Identify the preparation type.
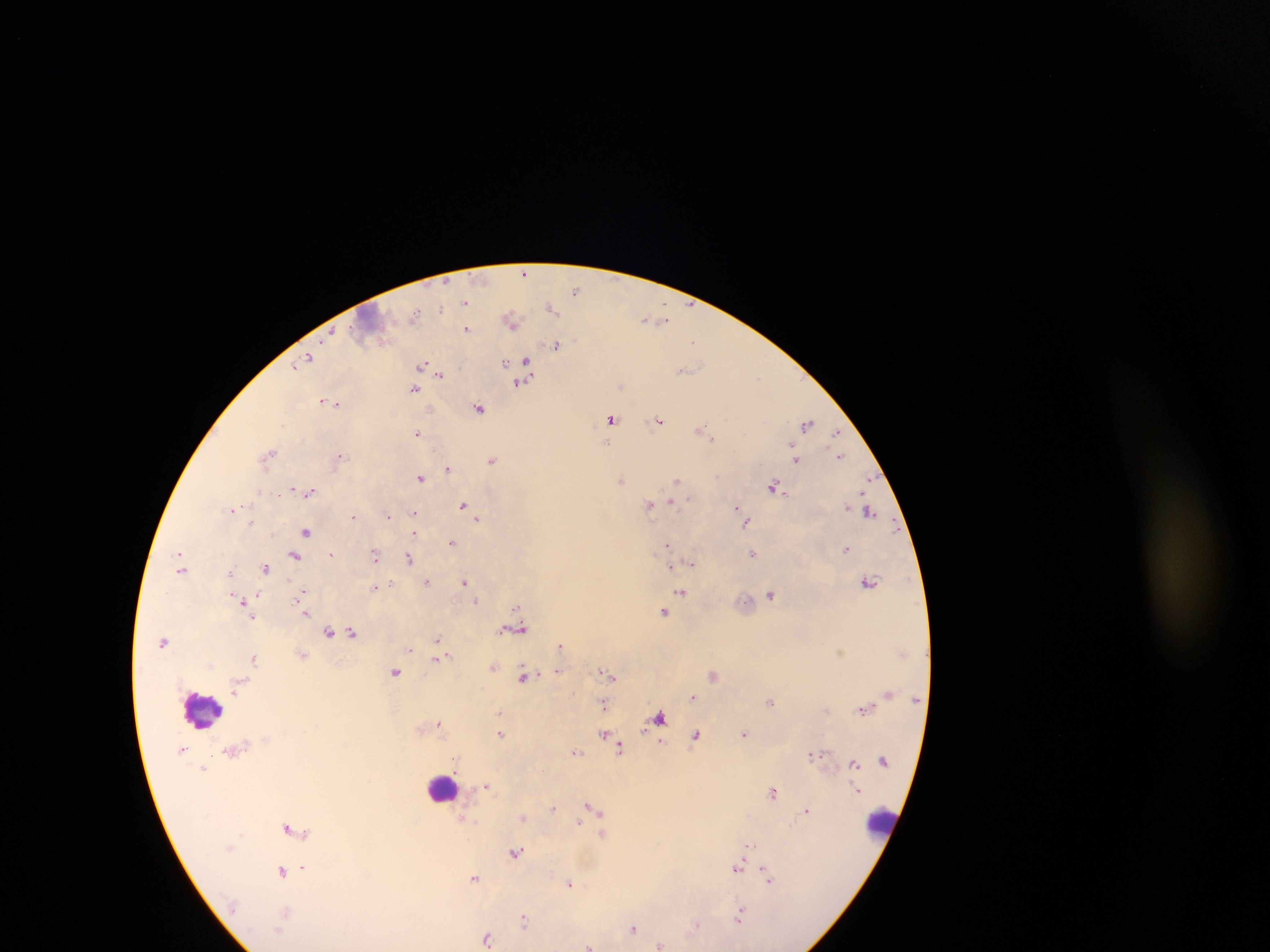

Thick blood film.

field_of_view: single
capture: mobile-phone photograph through a microscope
country: Ghana
image_size: 1270×952 pixels
malaria_parasite_locations: 'approximate centers as x y in pixels: 525 272; 576 290; 466 303; 550 307; 511 320; 649 320; 660 320; 467 328; 329 335; 693 341; 556 346; 308 357; 526 360; 505 363; 423 365; 295 366; 683 370; 440 376; 757 377; 519 383; 413 388; 322 401; 335 403; 479 408; 429 409; 612 418; 659 420; 807 423; 701 429; 836 431; 418 433; 712 439; 340 454; 269 455; 840 455; 795 458; 491 461; 447 468; 421 478; 621 478; 677 480; 870 480; 292 487; 774 487; 311 491; 688 500; 672 502; 463 505; 649 505; 846 505; 234 509; 737 509; 414 512; 870 512; 741 514; 353 516; 388 516; 477 519; 745 521; 251 523; 307 532; 413 534; 452 541; 667 545; 847 548; 331 554; 752 554; 374 555; 294 556; 408 559; 691 563; 266 568; 671 568; 181 569; 231 573; 464 581; 428 582; 869 582; 390 584; 374 587; 303 593; 682 593; 771 594; 475 600; 242 601; 514 607; 305 612; 664 612; 252 617; 517 629; 353 632; 329 633; 437 640; 164 642; 561 645; 840 653; 254 659; 436 659; 558 671; 395 672; 607 673; 713 675; 523 677; 693 697; 771 702; 603 704; 864 709; 500 713; 660 717; 438 724; 644 728; 501 733; 744 733; 604 734; 695 736; 661 742; 620 747; 577 752; 811 755; 455 759; 855 763; 204 769; 486 786; 774 791; 589 804; 554 808; 807 810; 523 818; 579 823; 287 828; 602 834; 749 844; 516 853; 302 867; 738 868; 282 870; 475 877; 768 878; 570 883; 739 917; 524 919; 696 925; 633 928; 487 938; 660 945; 588 946'
leukocyte_locations: 'approximate centers as x y in pixels: 374 316; 199 710; 443 788; 881 820'